Comment on the background quality.
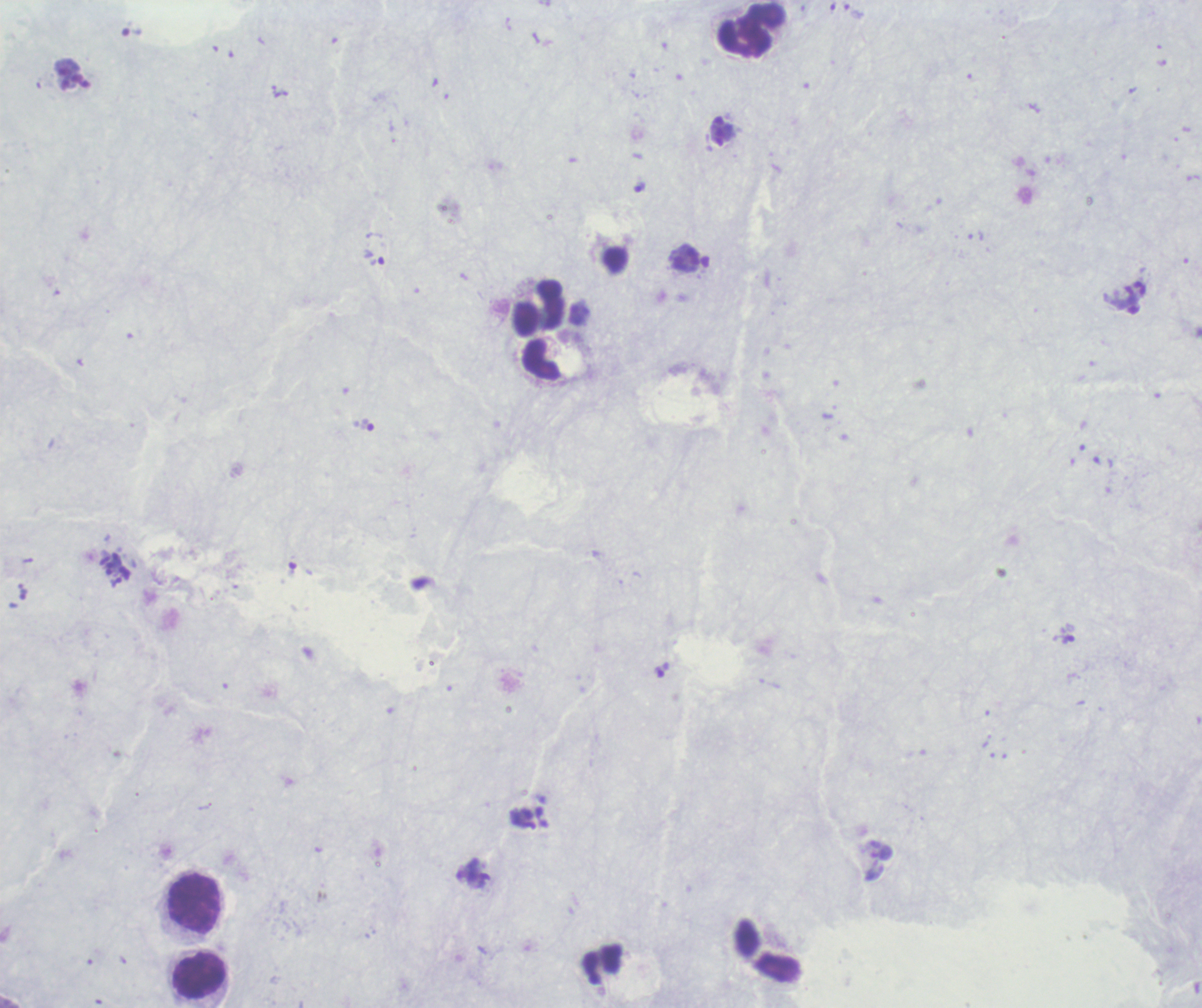

Poor.

coordinate format = approximate object centers, in pixels from the top-left corner
trophozoite locations = (x=854, y=11), (x=131, y=32), (x=1064, y=639)
leukocyte locations = (x=752, y=30), (x=540, y=307), (x=195, y=903), (x=199, y=976)
magnification = 100x
image size = 1202×1008 pixels
stain = Romanowsky
context = previously used in an actual diagnosis
field of view = one from this slide
preparation = thick blood film
result = malaria parasites detected